Assess this cell for malaria.
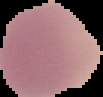
Uninfected.

image type = cell region segmented out of the field of view; surrounding area masked to black
preparation = thin blood film
image size = 103×97 pixels